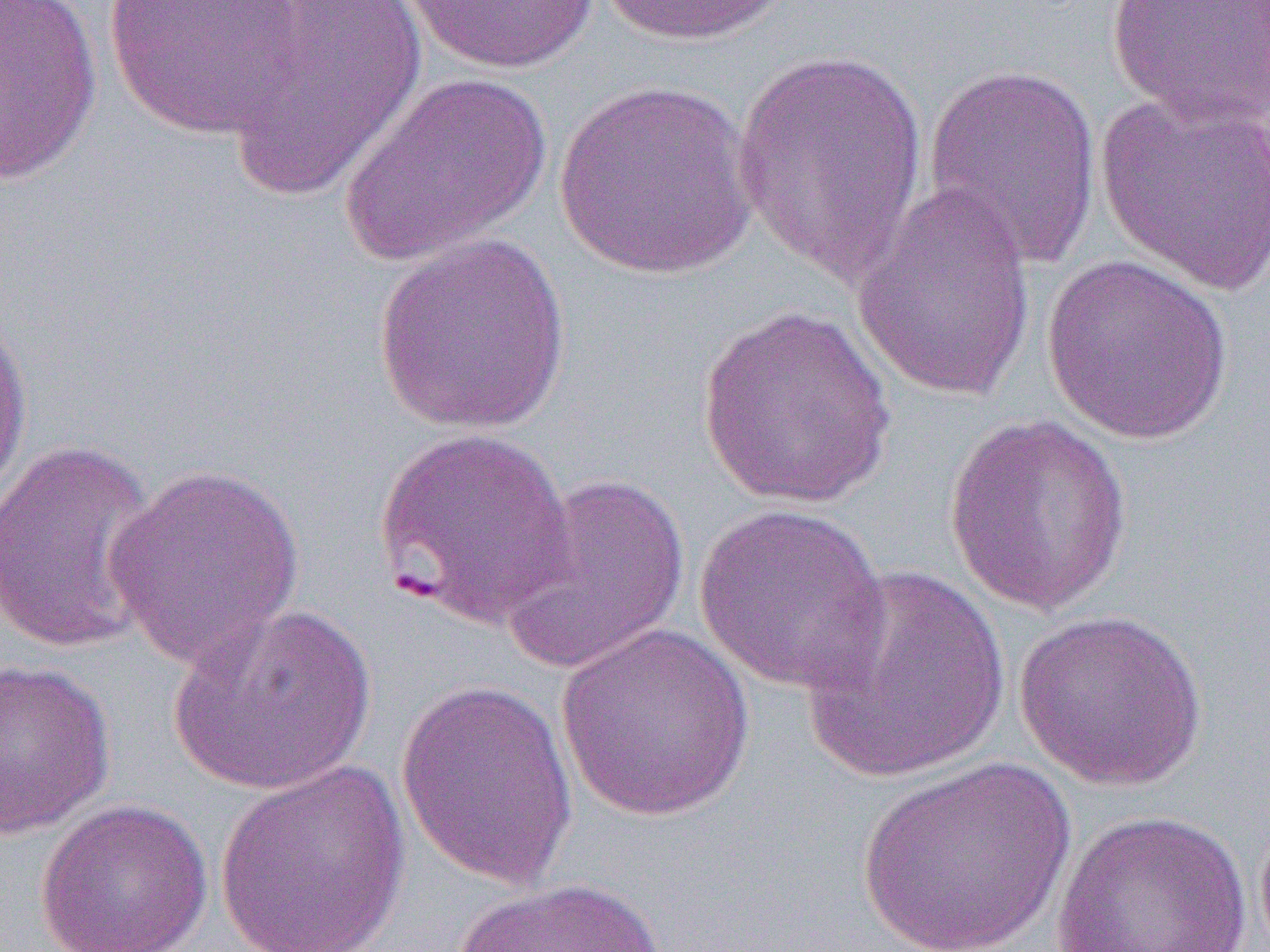

Approximate bounding boxes as (x1,y1)-(x2,y2) corner pairs in pixels. Uninfected red blood cell locations: (0,0)-(103,186), (103,0)-(308,138), (220,0)-(428,200), (595,0)-(791,47), (1106,0)-(1270,130), (399,1)-(603,76), (732,47)-(931,286), (923,63)-(1103,271), (340,71)-(553,267), (553,82)-(759,281), (1094,90)-(1270,296), (851,183)-(1038,405), (371,234)-(572,434), (1040,253)-(1235,447), (695,305)-(900,509), (0,307)-(35,509), (944,414)-(1135,616), (372,426)-(579,628), (0,439)-(164,656), (105,464)-(306,670), (499,472)-(691,680), (693,501)-(890,695), (799,562)-(1012,784), (167,599)-(379,797), (1012,609)-(1210,793), (555,624)-(757,821), (0,658)-(116,840), (394,677)-(580,888), (855,756)-(1077,952), (213,760)-(412,952), (34,798)-(214,952), (1051,810)-(1254,952), (447,877)-(670,952). Slide-level diagnosis: Plasmodium falciparum. Image is 1270×952 pixels. One field of a larger specimen. Captured at 1000x magnification. Optical microscopy. Thin blood film.